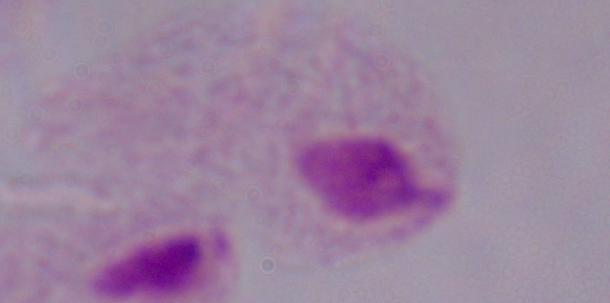
magnification = 1000x
identification = trichomonad
modality = micrograph